Name the blood parasite species.
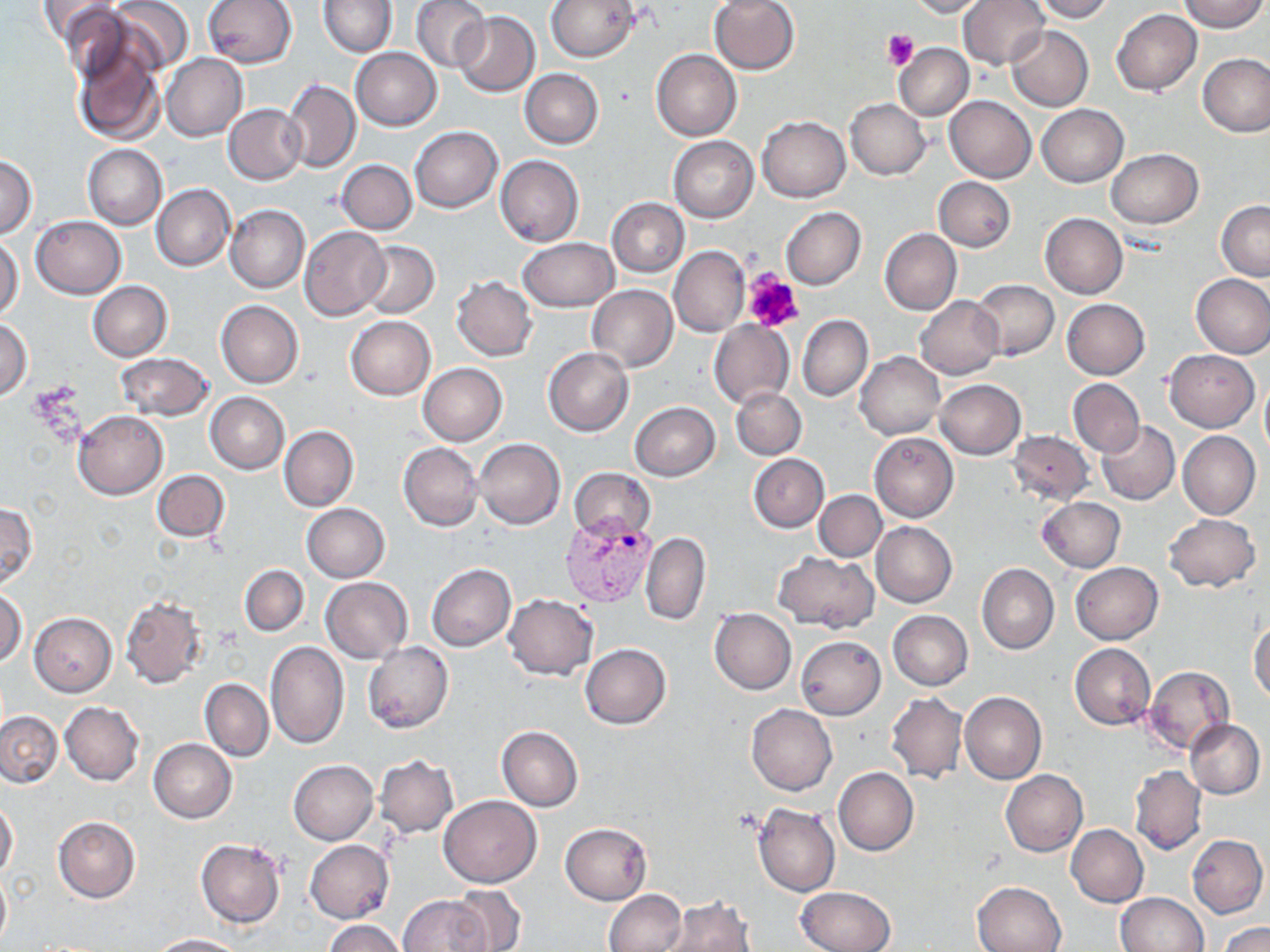
Plasmodium vivax.

Summary:
  - Coordinate format: approximate bounding boxes as [x1, y1, x2, y2] in pixels
  - Platelet locations: [882, 30, 919, 71], [743, 269, 804, 333]
  - Plasmodium vivax-infected red blood cell locations: [560, 512, 657, 607]
  - Uninfected red blood cell locations: [38, 0, 126, 59], [105, 0, 194, 76], [202, 0, 296, 68], [319, 0, 396, 57], [411, 0, 489, 72], [545, 0, 637, 62], [708, 0, 800, 74], [907, 0, 987, 18], [959, 0, 1049, 70], [1031, 0, 1114, 22], [1178, 0, 1267, 32], [1111, 8, 1202, 95], [453, 12, 539, 96], [1006, 26, 1093, 111], [71, 38, 167, 146], [894, 44, 973, 120], [350, 47, 442, 130], [652, 49, 741, 140], [162, 53, 246, 140], [1198, 53, 1270, 137], [520, 69, 603, 148], [283, 79, 360, 173], [944, 96, 1035, 182], [846, 99, 931, 181], [224, 104, 306, 184], [1036, 105, 1128, 187], [757, 116, 850, 202], [410, 126, 502, 212], [668, 136, 759, 222], [83, 144, 167, 229], [1106, 149, 1202, 228], [2, 154, 37, 239], [496, 156, 583, 247], [336, 159, 417, 234], [932, 177, 1016, 252], [152, 183, 235, 271], [607, 197, 689, 277], [1217, 201, 1270, 280], [226, 204, 309, 294], [781, 208, 865, 290], [1039, 213, 1128, 299], [31, 215, 126, 298], [1051, 215, 1136, 379], [299, 227, 390, 320], [879, 228, 961, 316], [0, 235, 23, 323], [517, 238, 619, 311], [360, 242, 438, 319], [669, 246, 748, 336], [1191, 274, 1270, 357], [452, 276, 538, 361], [970, 279, 1058, 361], [89, 281, 172, 360], [586, 285, 677, 373], [915, 296, 1003, 378], [1061, 299, 1150, 380], [216, 301, 304, 388], [797, 314, 873, 401], [345, 316, 435, 400], [1, 317, 33, 400], [708, 320, 794, 408], [543, 347, 633, 436], [1165, 350, 1259, 432], [855, 351, 945, 440], [115, 352, 215, 421], [418, 363, 508, 446], [1068, 378, 1144, 456], [935, 379, 1025, 459], [1260, 380, 1270, 459], [731, 386, 806, 460], [205, 392, 289, 474], [629, 402, 719, 480], [74, 410, 168, 500], [1097, 421, 1180, 504], [279, 425, 358, 511], [1008, 431, 1095, 505], [870, 432, 959, 523], [1177, 432, 1260, 519], [475, 438, 564, 529], [399, 442, 482, 532], [749, 454, 828, 532], [569, 468, 655, 541], [153, 470, 230, 544], [815, 490, 886, 561], [1038, 497, 1125, 573], [0, 502, 37, 589], [302, 504, 389, 582], [1163, 513, 1260, 592], [871, 522, 957, 607], [641, 531, 710, 625], [773, 551, 879, 632], [977, 562, 1059, 654], [1072, 562, 1163, 643], [427, 564, 516, 652], [240, 565, 309, 636], [321, 577, 411, 662], [0, 589, 27, 667], [504, 593, 598, 679], [121, 595, 208, 687], [709, 608, 796, 694], [888, 610, 972, 690], [28, 612, 118, 697], [1249, 619, 1270, 702], [796, 636, 886, 720], [266, 641, 349, 750], [363, 643, 454, 733], [1070, 643, 1155, 730], [581, 644, 670, 729], [1142, 666, 1234, 756], [200, 678, 274, 761], [886, 692, 967, 784], [960, 692, 1047, 784], [59, 701, 144, 785], [746, 704, 837, 795], [0, 711, 61, 787], [1186, 719, 1265, 798], [497, 725, 583, 810], [149, 740, 236, 823], [375, 755, 458, 838], [289, 760, 378, 845], [1130, 765, 1206, 855], [833, 768, 919, 856], [1002, 770, 1088, 857], [439, 795, 541, 888], [0, 800, 18, 881], [753, 804, 840, 896], [54, 816, 139, 903], [560, 822, 652, 905], [1066, 825, 1149, 907], [1187, 834, 1267, 918], [195, 838, 286, 928], [305, 840, 394, 923], [0, 869, 11, 948], [973, 881, 1067, 951], [797, 885, 895, 952], [451, 887, 525, 950], [604, 889, 686, 952], [1116, 892, 1208, 952], [397, 894, 493, 952], [662, 898, 754, 952], [325, 920, 404, 952], [1220, 922, 1270, 952], [149, 934, 246, 951]
  - Stain: May-Grünwald-Giemsa
  - Image size: 1270×952 pixels
  - Modality: light microscopy
  - Field of view: single
  - Preparation: thin blood film
  - Magnification: 1000x